Locate and identify every blood parasite.
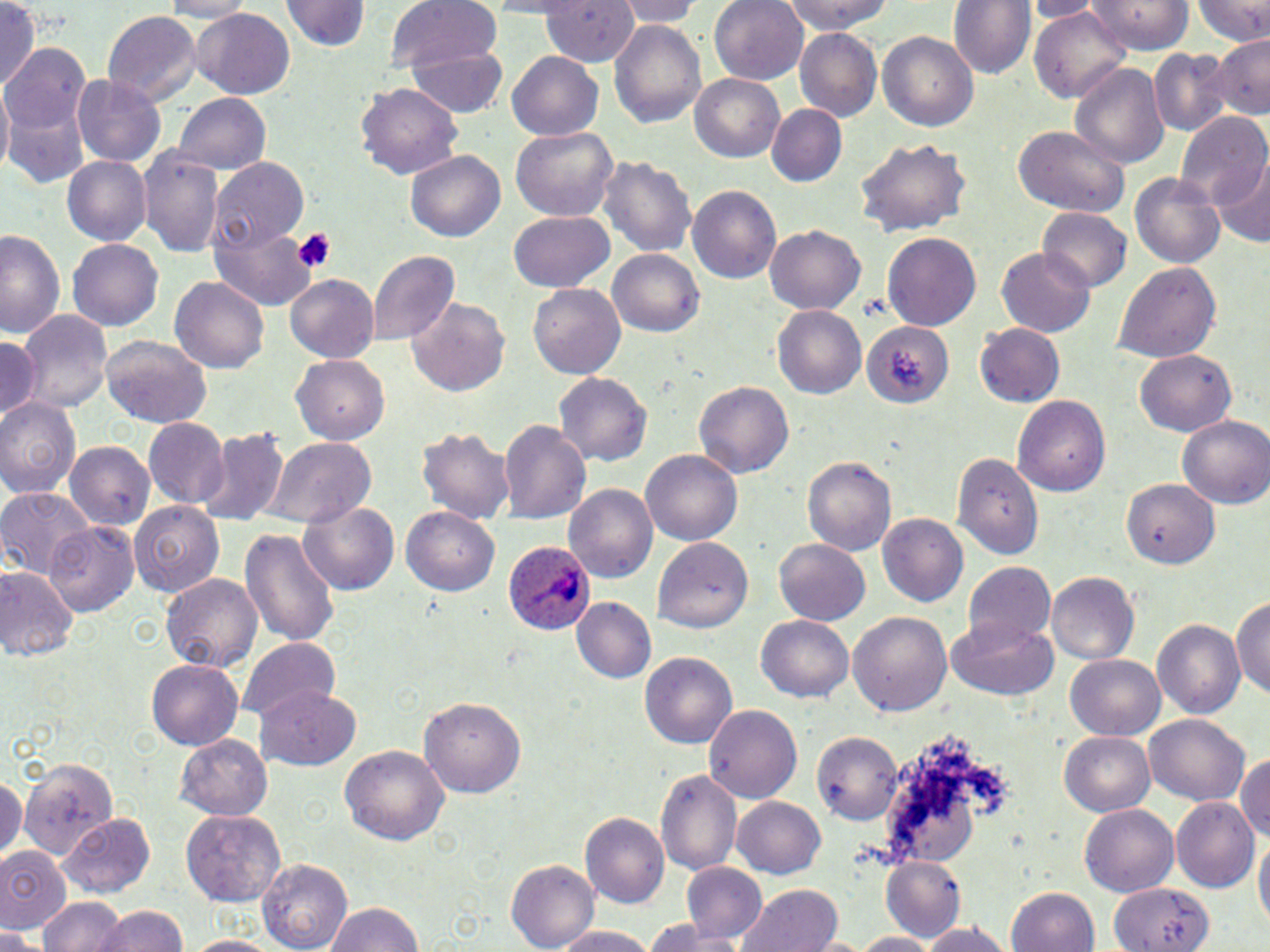
Approximate bounding boxes as named x1/y1/x2/y2 corners in pixels.
Plasmodium ovale-infected red blood cells: (x1=496, y1=536, x2=590, y2=640).
No Plasmodium falciparum, Plasmodium malariae, Plasmodium vivax, Babesia divergens, or Trypanosoma brucei observed.

Summary:
  - Uninfected red blood cell locations: (x1=0, y1=0, x2=41, y2=94), (x1=152, y1=0, x2=255, y2=20), (x1=288, y1=0, x2=367, y2=53), (x1=386, y1=0, x2=504, y2=76), (x1=542, y1=0, x2=640, y2=66), (x1=612, y1=0, x2=705, y2=26), (x1=709, y1=0, x2=809, y2=84), (x1=780, y1=0, x2=899, y2=34), (x1=949, y1=0, x2=1034, y2=81), (x1=1026, y1=0, x2=1100, y2=20), (x1=1089, y1=0, x2=1195, y2=53), (x1=1195, y1=0, x2=1270, y2=47), (x1=1028, y1=6, x2=1131, y2=104), (x1=189, y1=10, x2=295, y2=97), (x1=101, y1=12, x2=202, y2=108), (x1=610, y1=17, x2=707, y2=131), (x1=795, y1=28, x2=881, y2=121), (x1=877, y1=29, x2=979, y2=129), (x1=1209, y1=34, x2=1270, y2=121), (x1=3, y1=41, x2=92, y2=172), (x1=409, y1=44, x2=509, y2=117), (x1=1150, y1=48, x2=1234, y2=136), (x1=507, y1=53, x2=605, y2=139), (x1=1070, y1=62, x2=1169, y2=168), (x1=689, y1=73, x2=784, y2=163), (x1=72, y1=74, x2=165, y2=168), (x1=357, y1=80, x2=463, y2=179), (x1=1, y1=87, x2=13, y2=178), (x1=174, y1=93, x2=270, y2=176), (x1=767, y1=105, x2=844, y2=188), (x1=1179, y1=113, x2=1270, y2=216), (x1=1012, y1=127, x2=1128, y2=216), (x1=512, y1=128, x2=616, y2=220), (x1=853, y1=134, x2=971, y2=241), (x1=138, y1=145, x2=226, y2=260), (x1=406, y1=150, x2=506, y2=243), (x1=598, y1=153, x2=696, y2=259), (x1=61, y1=155, x2=150, y2=246), (x1=1212, y1=157, x2=1269, y2=247), (x1=212, y1=161, x2=307, y2=251), (x1=1131, y1=170, x2=1227, y2=270), (x1=687, y1=185, x2=779, y2=285), (x1=1038, y1=208, x2=1132, y2=292), (x1=509, y1=211, x2=614, y2=292), (x1=211, y1=219, x2=319, y2=309), (x1=765, y1=222, x2=865, y2=313), (x1=0, y1=229, x2=63, y2=341), (x1=883, y1=232, x2=980, y2=333), (x1=68, y1=239, x2=164, y2=329), (x1=995, y1=246, x2=1096, y2=338), (x1=366, y1=249, x2=460, y2=346), (x1=610, y1=249, x2=706, y2=338), (x1=1116, y1=261, x2=1220, y2=364), (x1=170, y1=273, x2=270, y2=374), (x1=285, y1=274, x2=378, y2=362), (x1=529, y1=283, x2=625, y2=381), (x1=407, y1=298, x2=509, y2=397), (x1=772, y1=304, x2=867, y2=399), (x1=16, y1=307, x2=114, y2=413), (x1=863, y1=323, x2=949, y2=409), (x1=976, y1=323, x2=1066, y2=408), (x1=0, y1=335, x2=39, y2=422), (x1=100, y1=335, x2=214, y2=426), (x1=1136, y1=351, x2=1235, y2=436), (x1=290, y1=355, x2=390, y2=445), (x1=552, y1=370, x2=654, y2=469), (x1=693, y1=381, x2=793, y2=478), (x1=1014, y1=395, x2=1112, y2=497), (x1=0, y1=396, x2=82, y2=498), (x1=143, y1=417, x2=228, y2=507), (x1=1178, y1=417, x2=1270, y2=508), (x1=499, y1=418, x2=592, y2=528), (x1=194, y1=426, x2=288, y2=527), (x1=417, y1=428, x2=514, y2=525), (x1=259, y1=436, x2=377, y2=529), (x1=65, y1=441, x2=154, y2=531), (x1=642, y1=450, x2=741, y2=546), (x1=951, y1=450, x2=1041, y2=558), (x1=803, y1=455, x2=895, y2=555), (x1=1121, y1=475, x2=1218, y2=567), (x1=564, y1=485, x2=656, y2=584), (x1=0, y1=487, x2=95, y2=578), (x1=298, y1=498, x2=402, y2=596), (x1=131, y1=501, x2=225, y2=595), (x1=402, y1=506, x2=500, y2=598), (x1=878, y1=513, x2=967, y2=607), (x1=44, y1=522, x2=139, y2=619), (x1=239, y1=526, x2=340, y2=648), (x1=650, y1=538, x2=753, y2=629), (x1=773, y1=538, x2=871, y2=627), (x1=965, y1=560, x2=1056, y2=650), (x1=0, y1=565, x2=78, y2=663), (x1=163, y1=572, x2=261, y2=674), (x1=1047, y1=573, x2=1138, y2=665), (x1=1232, y1=593, x2=1270, y2=702), (x1=570, y1=598, x2=656, y2=686), (x1=849, y1=610, x2=951, y2=718), (x1=757, y1=615, x2=853, y2=702), (x1=950, y1=616, x2=1058, y2=701), (x1=1151, y1=620, x2=1245, y2=720), (x1=236, y1=636, x2=341, y2=723), (x1=641, y1=651, x2=737, y2=748), (x1=1066, y1=653, x2=1165, y2=739), (x1=147, y1=659, x2=243, y2=751), (x1=255, y1=686, x2=361, y2=771), (x1=417, y1=697, x2=526, y2=800), (x1=705, y1=704, x2=802, y2=804), (x1=1146, y1=714, x2=1248, y2=805), (x1=814, y1=729, x2=905, y2=824), (x1=1058, y1=730, x2=1156, y2=816), (x1=176, y1=735, x2=270, y2=818), (x1=339, y1=745, x2=450, y2=846), (x1=1234, y1=748, x2=1270, y2=850), (x1=20, y1=759, x2=116, y2=863), (x1=654, y1=766, x2=742, y2=873), (x1=0, y1=773, x2=24, y2=862), (x1=732, y1=797, x2=828, y2=878), (x1=1171, y1=800, x2=1256, y2=893), (x1=1082, y1=803, x2=1177, y2=895), (x1=181, y1=810, x2=288, y2=907), (x1=60, y1=812, x2=155, y2=897), (x1=580, y1=813, x2=670, y2=910), (x1=1254, y1=833, x2=1269, y2=935), (x1=0, y1=845, x2=66, y2=933), (x1=880, y1=857, x2=968, y2=942), (x1=505, y1=859, x2=596, y2=952), (x1=258, y1=860, x2=351, y2=950), (x1=681, y1=863, x2=767, y2=946), (x1=1111, y1=881, x2=1212, y2=952), (x1=739, y1=886, x2=844, y2=952), (x1=1007, y1=888, x2=1101, y2=952), (x1=39, y1=896, x2=126, y2=952), (x1=321, y1=901, x2=425, y2=952), (x1=89, y1=906, x2=190, y2=952), (x1=640, y1=920, x2=738, y2=951), (x1=917, y1=923, x2=1012, y2=952), (x1=550, y1=925, x2=663, y2=950), (x1=0, y1=927, x2=45, y2=952), (x1=848, y1=931, x2=947, y2=951), (x1=179, y1=935, x2=288, y2=952)
  - Platelet locations: (x1=292, y1=229, x2=338, y2=277)
  - Slide-level diagnosis: Plasmodium ovale
  - Image size: 1270×952 pixels
  - Modality: optical microscopy
  - Preparation: thin blood smear
  - Field of view: one of a larger specimen
  - Magnification: 1000x
  - Stain: May-Grünwald-Giemsa